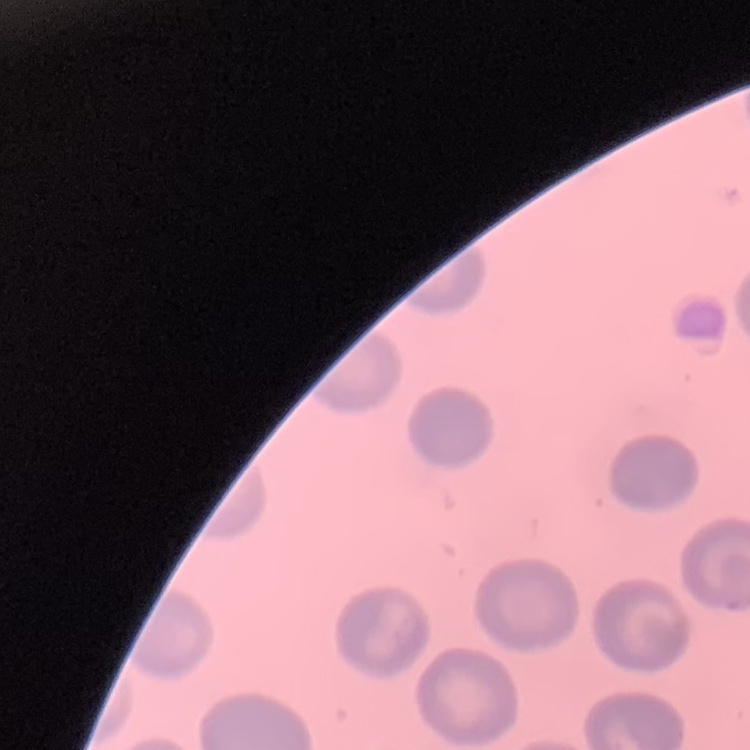

Summary:
  - Erythrocyte morphology: no rouleaux formation
  - Stain: Field's or Giemsa
  - Image type: square crop of a larger photomicrograph
  - Preparation: thin blood film